Report the malaria status of this cell.
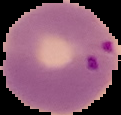

Parasitized.

preparation = thin blood film
image type = cell region segmented out of the field of view; surrounding area masked to black
image size = 121×115 pixels